Classify this cell by malaria status.
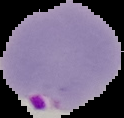
It is parasitized.

Image is 124×118 pixels. From a thin blood smear. Segmented cell region on a black background.